Report the malaria status of this cell.
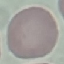

Uninfected.

Thin smear of blood. Giemsa-stained preparation. Photographed with a smartphone camera at the microscope eyepiece. Automatically extracted cell patch, resized to 64 × 64 pixels.